Classify this cell by malaria status.
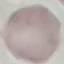
Uninfected.

Summary:
  - Stain: Giemsa
  - Preparation: thin blood smear
  - Capture: smartphone through the microscope eyepiece
  - Image type: automatically extracted cell patch, resized to 64 × 64 pixels